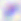 Captured at 400x magnification. Toxoplasma gondii is seen. Photomicrograph.